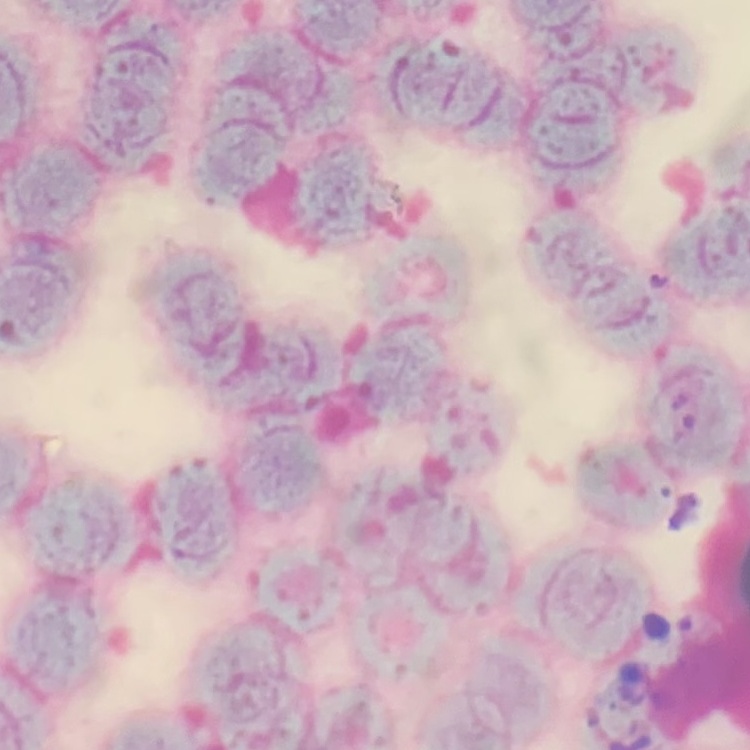

Summary:
  - Erythrocyte morphology: rouleaux formation
  - Preparation: thin blood smear
  - Stain: Field's or Giemsa
  - Image type: one tile cut from a larger photomicrograph